State the preparation type.
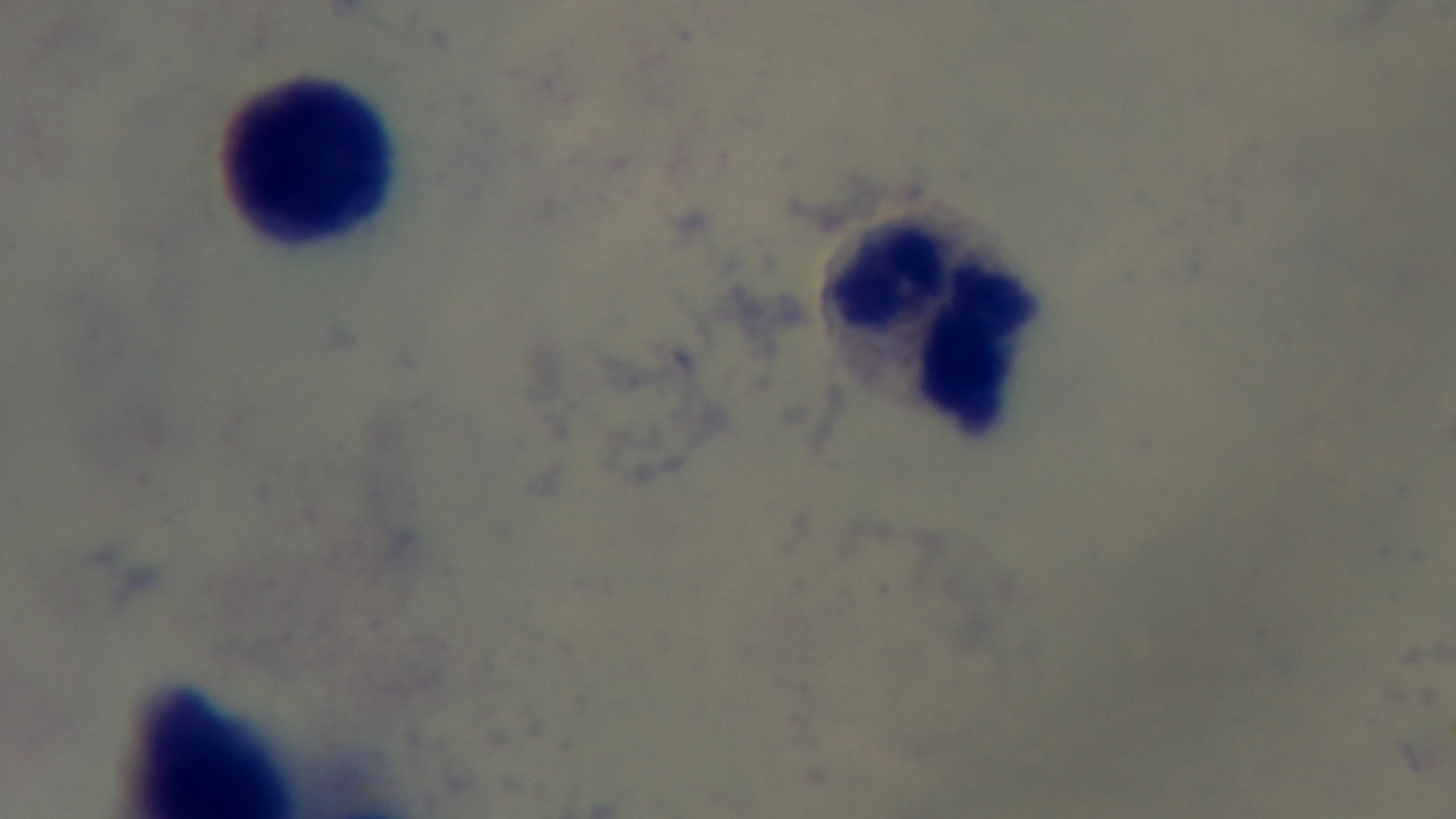
Thick.

Oil-immersion objective, 100x. Mounted 4K digital camera. Photomicrograph. One field from the slide. Malaria status: negative. Giemsa-stained.